Assess the morphology of the red blood cells.
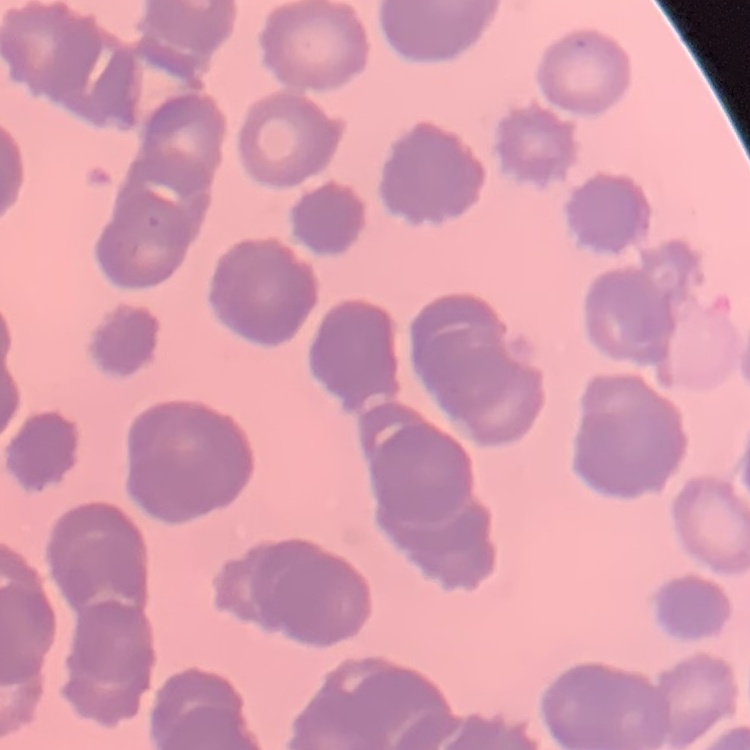

They show rouleaux formation.

preparation = thin blood film
image type = one tile cut from a larger photomicrograph
stain = Field's or Giemsa